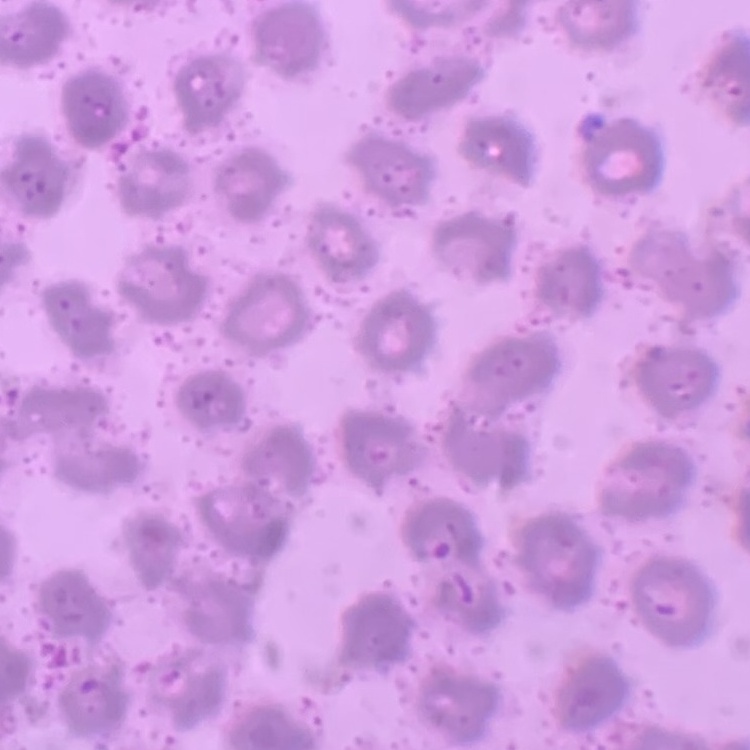
The red blood cells show no rouleaux formation. Thin blood smear. One tile cut from a larger photomicrograph. Stained with either Field's or Giemsa.